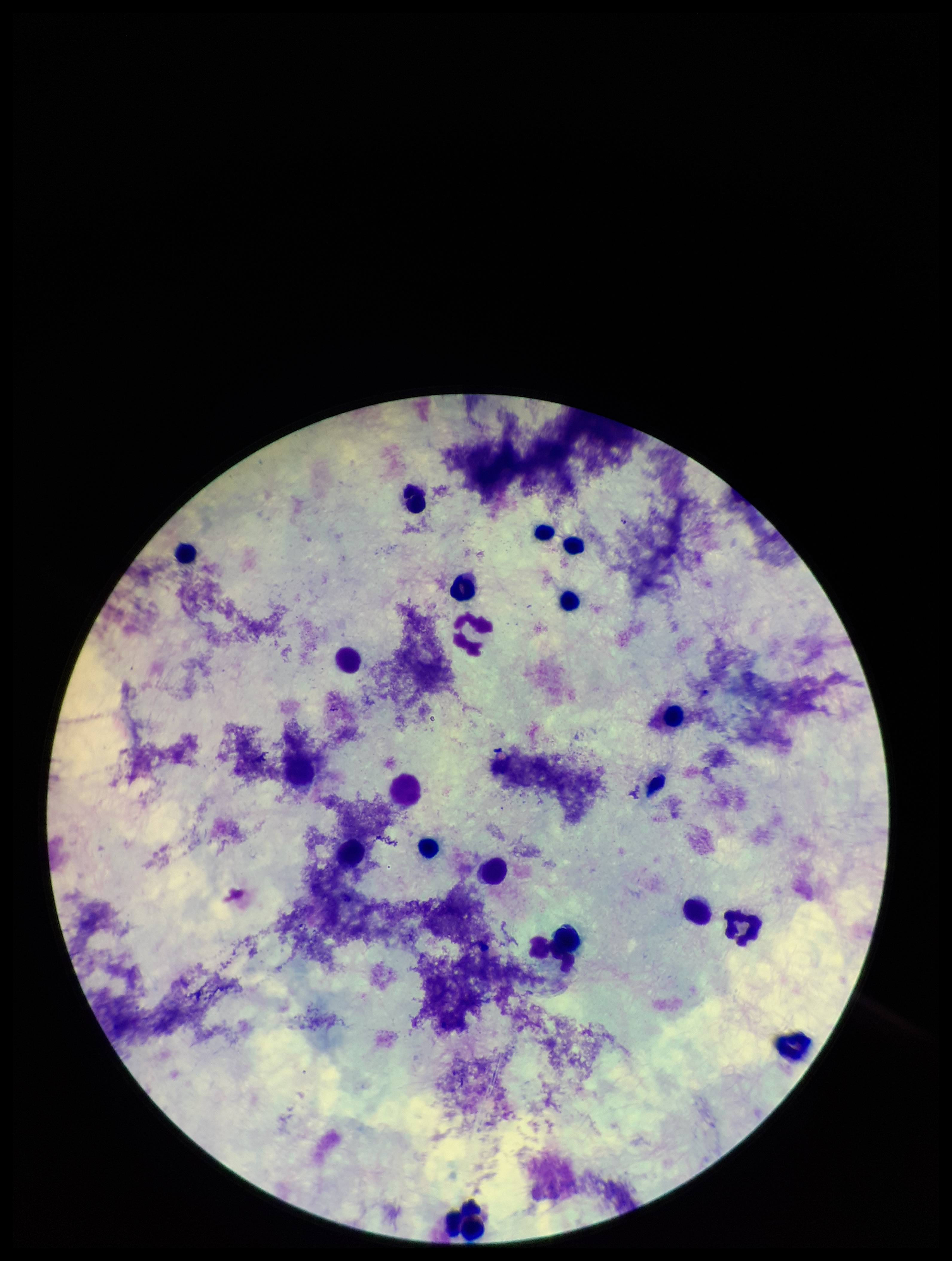

{
  "patient_malaria_status": "negative",
  "leukocyte_count": 17,
  "stain": "Giemsa",
  "capture": "smartphone photograph through the microscope eyepiece",
  "plasmodium_parasites": "none detected",
  "image_size": "952×1261 pixels",
  "preparation": "thick blood smear",
  "field_of_view": "single",
  "parasite_count": 0
}